Evaluate for malaria.
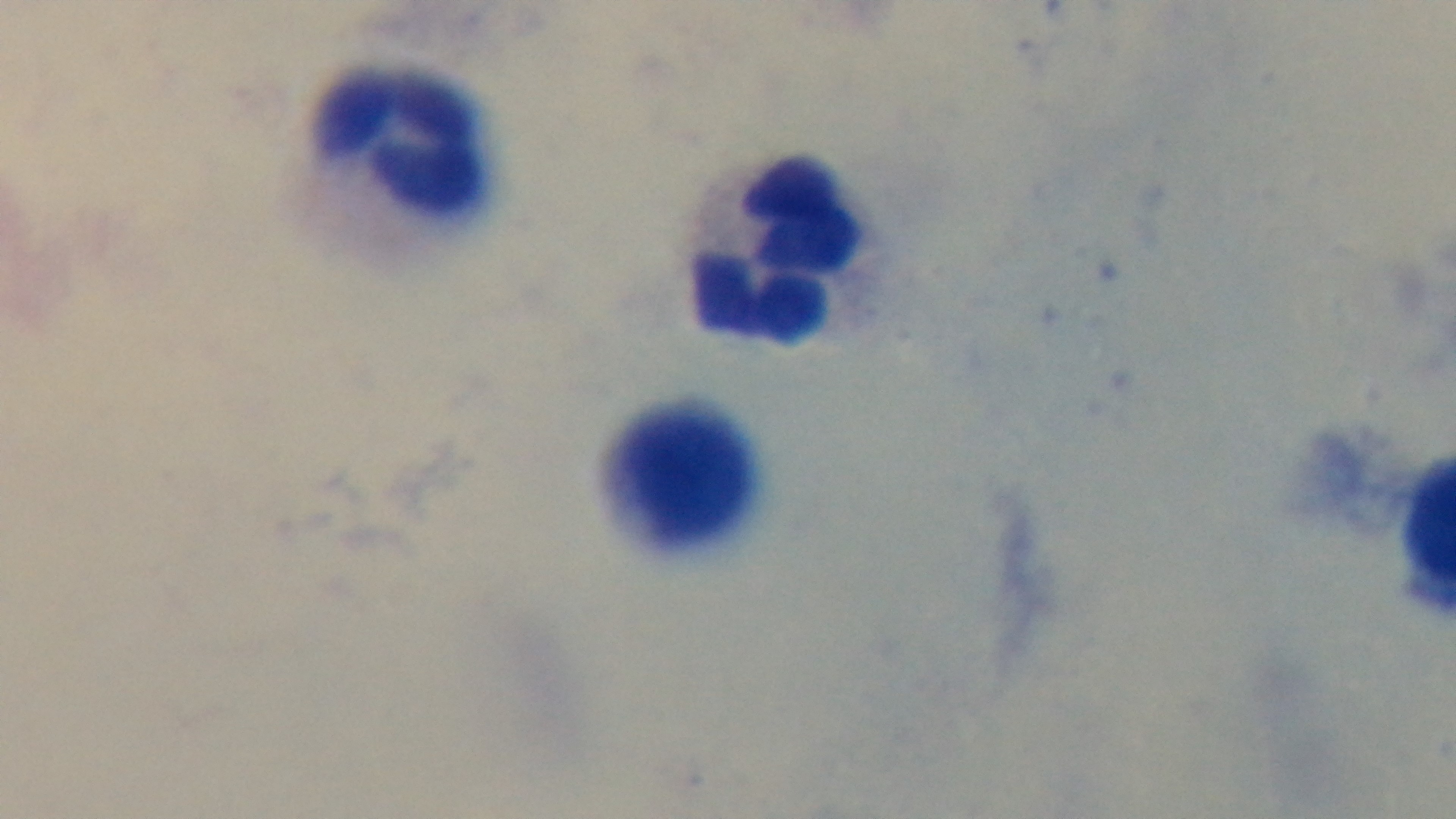
Negative.

Giemsa-stained. Oil-immersion objective, 100x. Photomicrograph. Preparation: thick smear. Captured with a mounted 4K digital camera. One field from the slide.